Locate every blood parasite and identify its species.
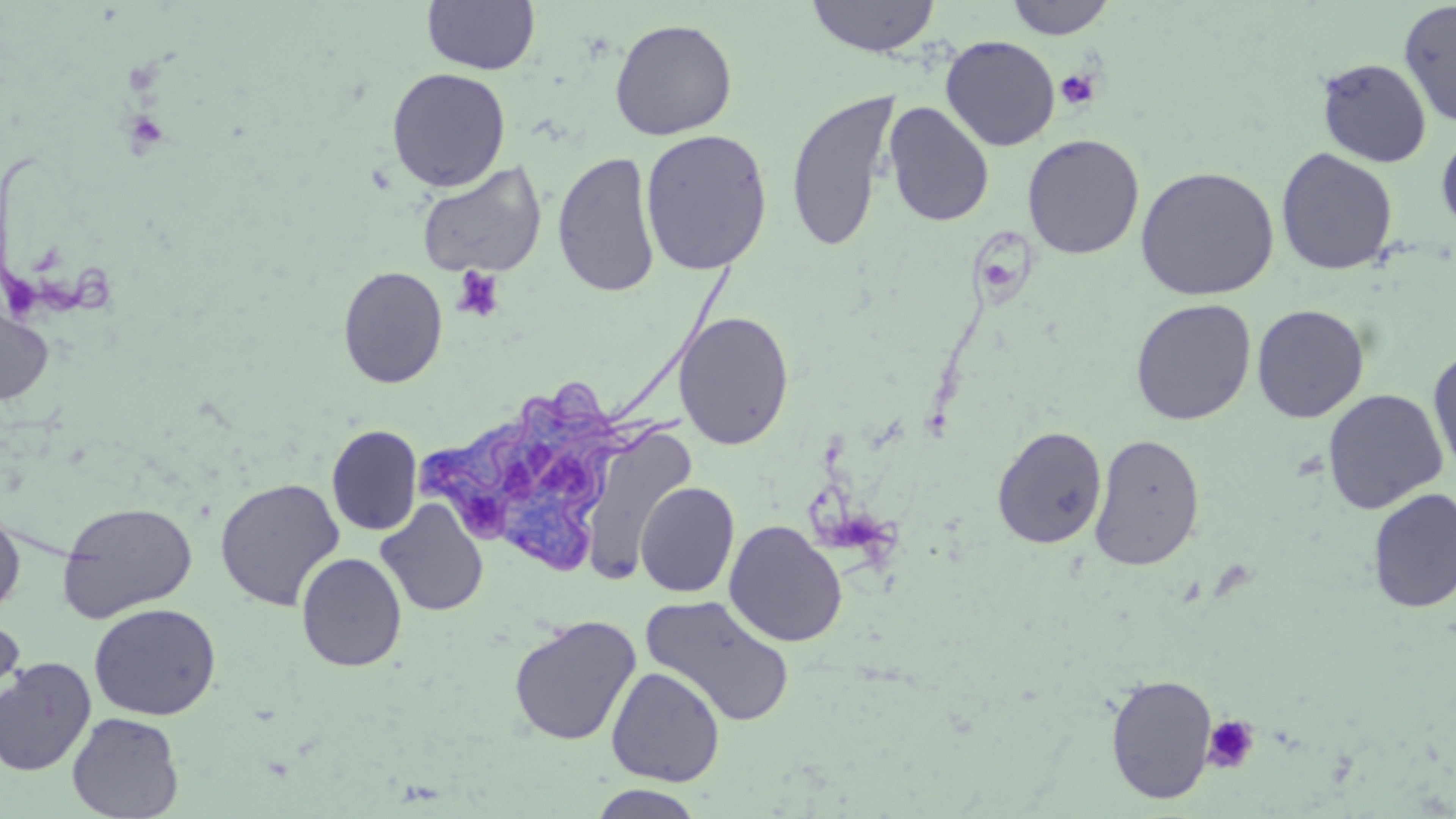

Approximate bounding boxes as (x1, y1, x2, y2) in pixels.
Trypanosoma brucei: (415, 349, 687, 580).
No Plasmodium falciparum, Plasmodium ovale, Plasmodium malariae, Plasmodium vivax, or Babesia divergens observed.

Uninfected red blood cell locations: (806, 0, 941, 57), (1005, 0, 1115, 40), (422, 1, 540, 75), (1399, 1, 1456, 129), (609, 18, 737, 141), (940, 35, 1060, 151), (1316, 58, 1432, 167), (387, 67, 511, 192), (784, 89, 900, 252), (882, 101, 995, 227), (639, 128, 773, 276), (1436, 130, 1456, 235), (1022, 134, 1145, 259), (1275, 147, 1398, 275), (552, 151, 661, 297), (417, 162, 547, 278), (1135, 165, 1280, 301), (338, 265, 448, 388), (0, 298, 55, 407), (1131, 298, 1256, 425), (1251, 304, 1369, 423), (674, 311, 794, 450), (1427, 345, 1456, 477), (1322, 388, 1448, 514), (326, 425, 423, 536), (992, 425, 1108, 549), (581, 426, 697, 586), (1089, 433, 1205, 571), (215, 478, 345, 611), (636, 481, 740, 598), (1367, 487, 1456, 614), (376, 499, 489, 617), (57, 501, 198, 623), (0, 507, 25, 616), (723, 520, 848, 647), (296, 552, 407, 672), (640, 594, 796, 728), (89, 603, 221, 720), (0, 614, 24, 713), (509, 615, 641, 746), (0, 658, 96, 776), (606, 666, 725, 786), (1105, 673, 1218, 804), (67, 711, 184, 819), (588, 784, 707, 819). Platelet locations: (1055, 67, 1100, 111), (451, 267, 504, 321), (1203, 714, 1259, 773). Slide-level diagnosis: Trypanosoma brucei. Thin blood film. Captured at 1000x magnification. Single field of view. Optical microscopy. May-Grünwald-Giemsa-stained preparation. Image is 1456×819 pixels.